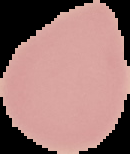

Summary:
  - Image type: segmented cell region with the area outside set to black
  - Malaria status: uninfected
  - Preparation: thin blood smear
  - Image size: 130×154 pixels